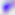
Captured at 400x magnification. Toxoplasma gondii is seen. Photomicrograph.